Point out each leukocyte.
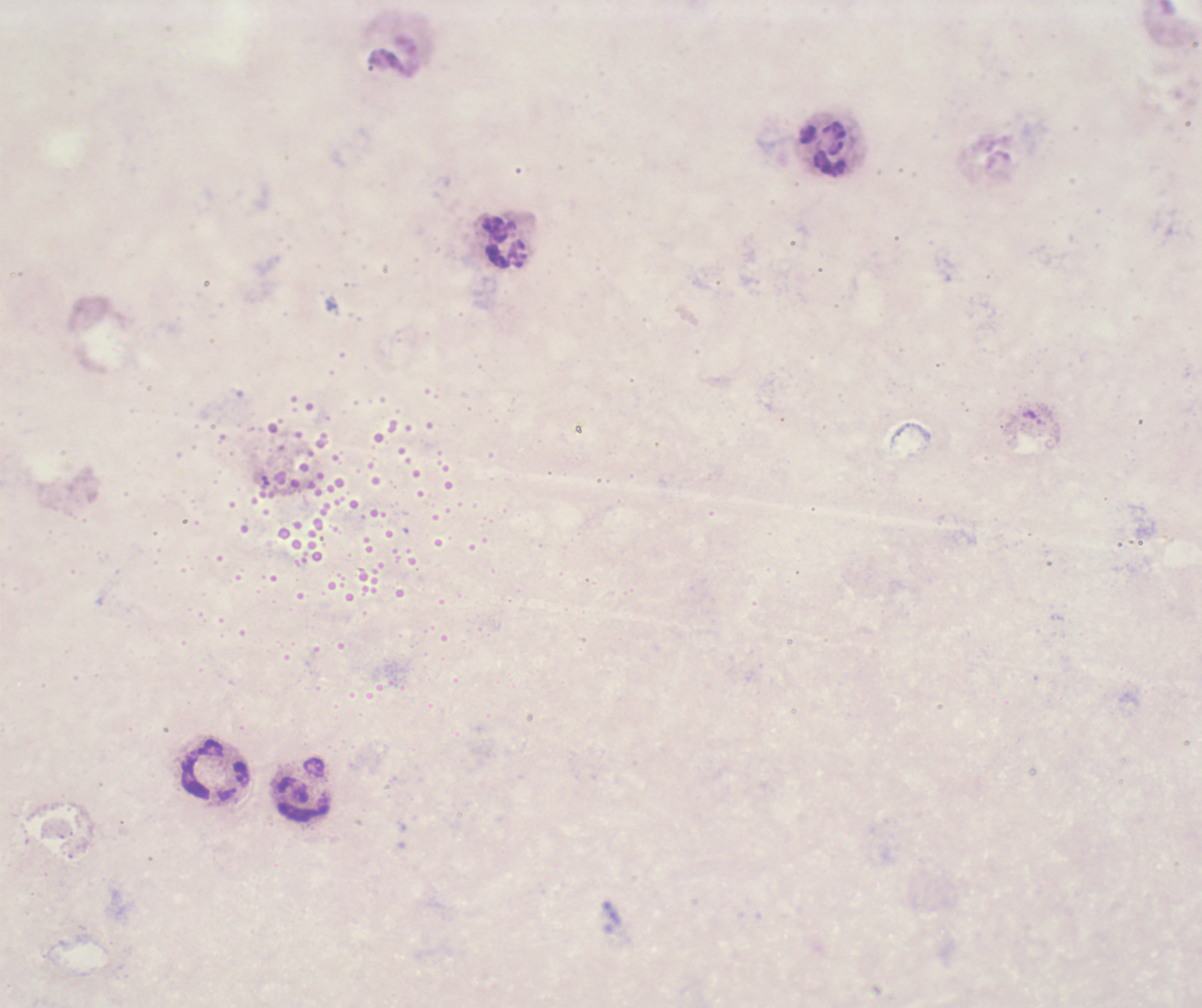

Approximate object centers, in pixels from the top-left corner.
Leukocytes: (x=824, y=149), (x=504, y=243), (x=214, y=770), (x=304, y=790).

Summary:
  - Field of view: one from this slide
  - Result: negative for Plasmodium parasites
  - Magnification: 100x
  - Context: previously used in a real diagnosis
  - Background quality: poor
  - Image size: 1202×1008 pixels
  - Coloration quality: bad
  - Preparation: thick smear of blood
  - Stain: Romanowsky